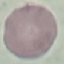
Summary:
  - Malaria status: uninfected
  - Stain: Giemsa
  - Preparation: thin smear
  - Capture: smartphone through the microscope eyepiece
  - Image type: automatically extracted cell patch, resized to 64 × 64 pixels